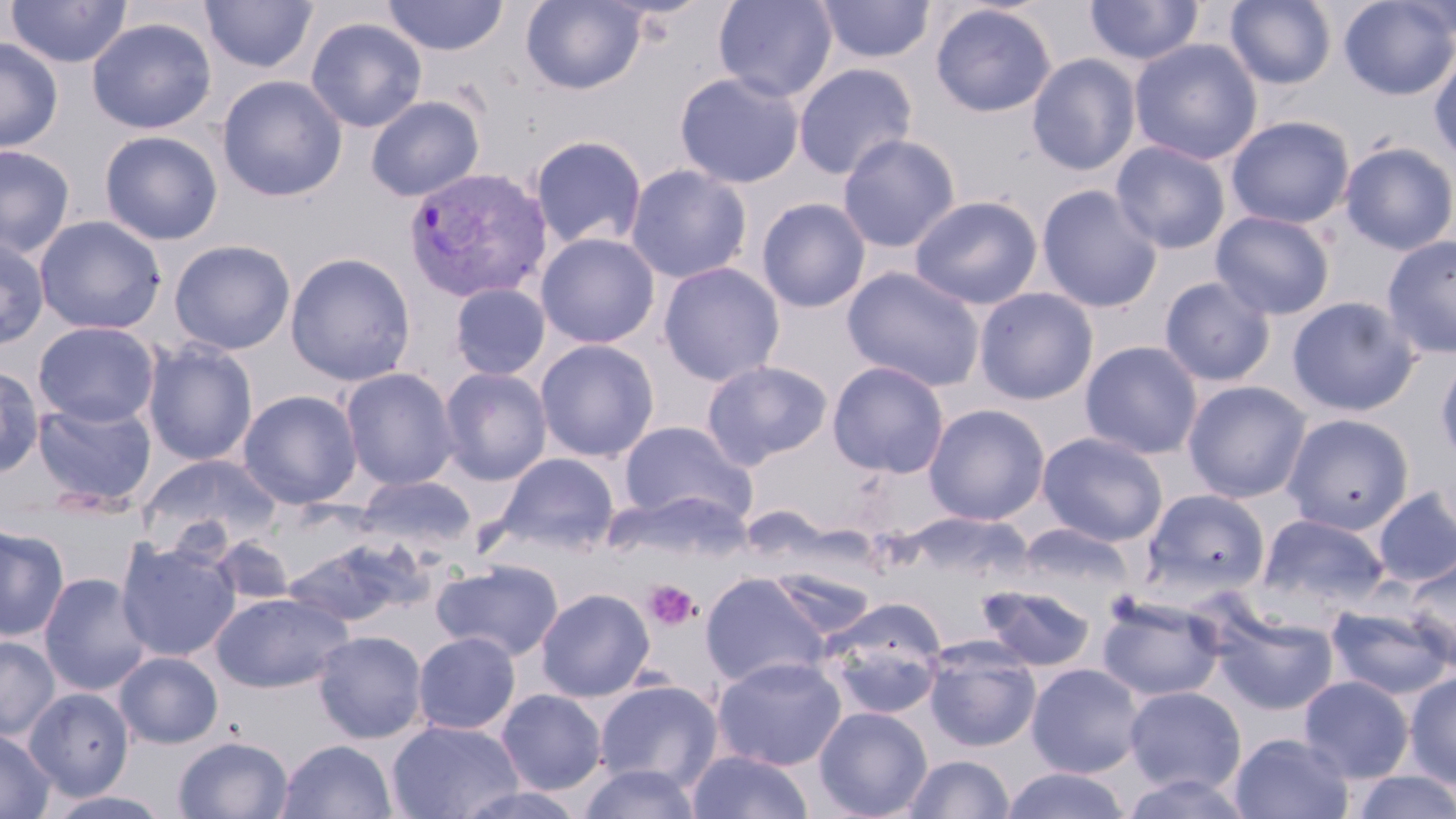
Summary:
  - Coordinate format: approximate bounding boxes as (x1, y1, x2, y2) in pixels
  - Plasmodium vivax-infected red blood cell locations: (403, 168, 552, 304)
  - Uninfected red blood cell locations: (200, 0, 319, 74), (383, 0, 508, 56), (521, 0, 646, 95), (713, 0, 838, 102), (1084, 0, 1205, 66), (1225, 0, 1336, 89), (1338, 0, 1456, 100), (1396, 0, 1456, 43), (3, 1, 133, 68), (815, 1, 935, 65), (929, 3, 1057, 118), (87, 17, 217, 134), (305, 17, 428, 133), (0, 37, 63, 153), (1128, 38, 1263, 165), (1429, 50, 1456, 164), (1027, 53, 1141, 176), (793, 62, 918, 180), (674, 71, 805, 189), (217, 75, 347, 202), (366, 96, 484, 201), (1225, 116, 1355, 229), (99, 130, 223, 245), (837, 133, 961, 252), (530, 135, 647, 251), (1111, 140, 1231, 255), (1339, 141, 1456, 254), (0, 145, 75, 258), (625, 164, 752, 283), (1036, 184, 1163, 313), (909, 194, 1044, 310), (756, 197, 871, 313), (1210, 210, 1336, 320), (34, 215, 165, 335), (536, 232, 660, 348), (0, 235, 49, 350), (1382, 235, 1456, 359), (168, 240, 296, 355), (284, 252, 416, 386), (658, 261, 785, 386), (843, 266, 985, 392), (1159, 276, 1276, 387), (449, 283, 551, 380), (973, 287, 1100, 406), (1287, 296, 1421, 417), (34, 321, 160, 427), (535, 339, 660, 462), (142, 340, 258, 466), (1080, 341, 1203, 459), (1435, 352, 1456, 469), (701, 360, 833, 469), (827, 361, 950, 478), (0, 364, 44, 478), (340, 367, 459, 491), (439, 367, 552, 485), (1183, 380, 1311, 503), (238, 389, 362, 509), (33, 399, 157, 511), (923, 403, 1050, 526), (1282, 413, 1414, 535), (618, 421, 757, 528), (1037, 431, 1168, 546), (138, 453, 281, 557), (494, 453, 620, 555), (354, 474, 475, 553), (1372, 487, 1456, 588), (1142, 488, 1271, 600), (742, 505, 832, 562), (1257, 514, 1390, 613), (1016, 522, 1136, 611), (0, 523, 69, 641), (210, 536, 295, 606), (282, 536, 432, 628), (116, 539, 241, 662), (1402, 556, 1456, 670), (431, 559, 564, 661), (772, 570, 876, 639), (699, 571, 832, 689), (38, 572, 152, 696), (978, 584, 1096, 672), (536, 587, 655, 701), (211, 591, 352, 693), (1096, 595, 1224, 702), (818, 600, 947, 717), (1326, 602, 1454, 700), (1212, 609, 1339, 716), (313, 630, 428, 743), (413, 631, 521, 735), (0, 635, 60, 740), (923, 641, 1041, 752), (114, 651, 223, 749), (712, 656, 848, 772), (1026, 663, 1145, 778), (1404, 671, 1456, 788), (1298, 675, 1414, 783), (593, 679, 723, 791), (1124, 686, 1246, 795), (24, 687, 134, 801), (495, 688, 607, 795), (814, 706, 933, 819), (386, 719, 524, 819), (0, 728, 55, 818), (1229, 732, 1354, 819), (173, 735, 293, 819), (277, 739, 397, 819), (686, 750, 814, 819), (901, 755, 1015, 818), (576, 763, 703, 819), (1000, 768, 1131, 819), (1348, 771, 1456, 818), (448, 783, 589, 819), (43, 790, 174, 819)
  - Platelet locations: (643, 579, 701, 631)
  - Slide-level diagnosis: Plasmodium vivax
  - Magnification: 1000x
  - Stain: May-Grünwald-Giemsa
  - Field of view: single
  - Preparation: thin blood smear
  - Image size: 1456×819 pixels
  - Modality: light microscopy